State the preparation type.
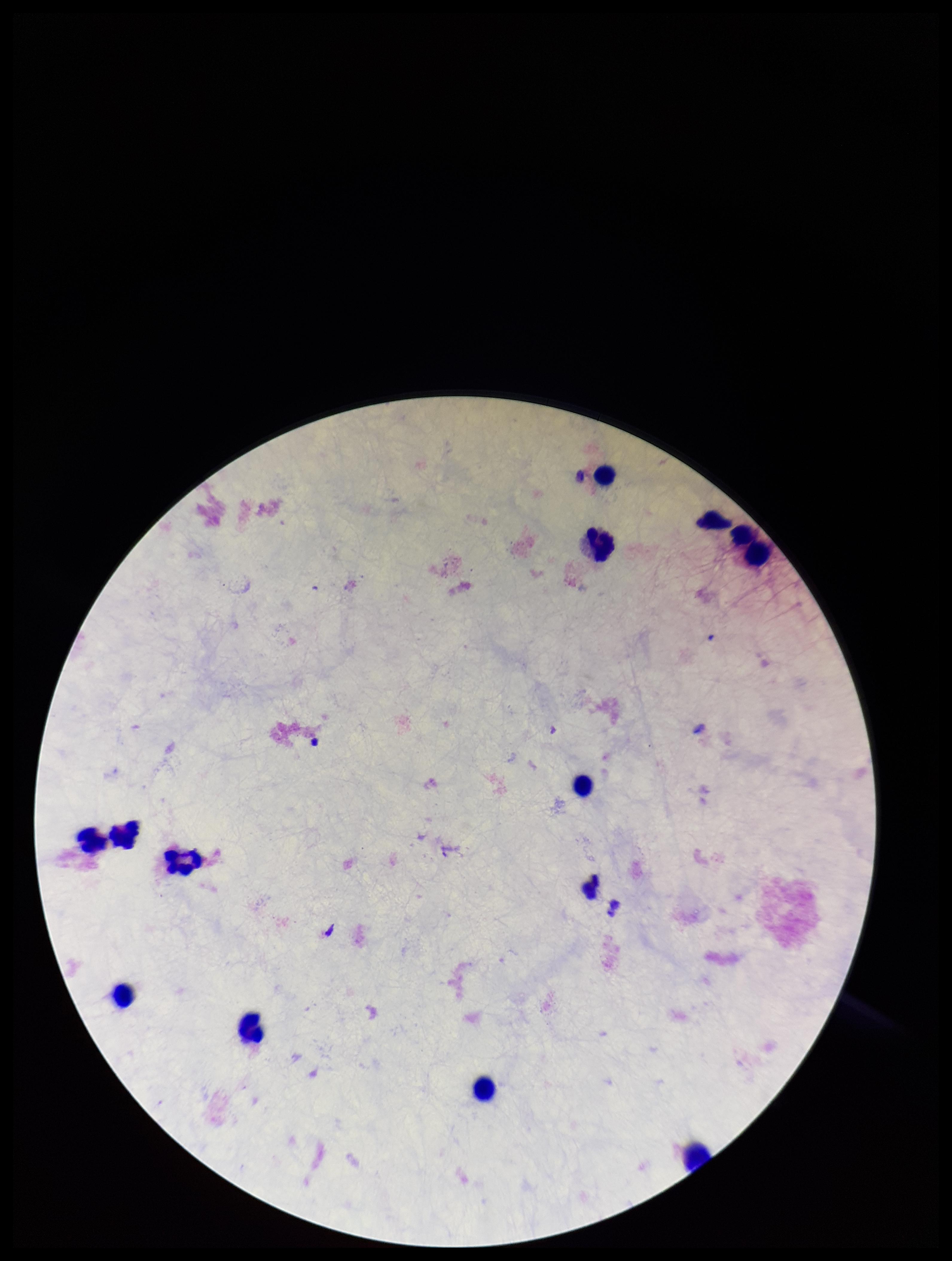

A thick smear.

{
  "plasmodium_parasites": "none seen",
  "field_of_view": "single",
  "stain": "Giemsa",
  "patient_malaria_status": "negative",
  "parasite_count": 0,
  "capture": "smartphone photograph through the microscope eyepiece",
  "image_size": "952×1261 pixels",
  "leukocyte_count": 13
}